Classify this cell by malaria status.
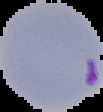

It is parasitized.

Cell region segmented out of the field of view; the surrounding area is masked to black. From a thin blood smear. Image is 103×112 pixels.